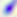

Summary:
  - Modality: micrograph
  - Magnification: 400x
  - Identification: Toxoplasma gondii